State the blood parasite species.
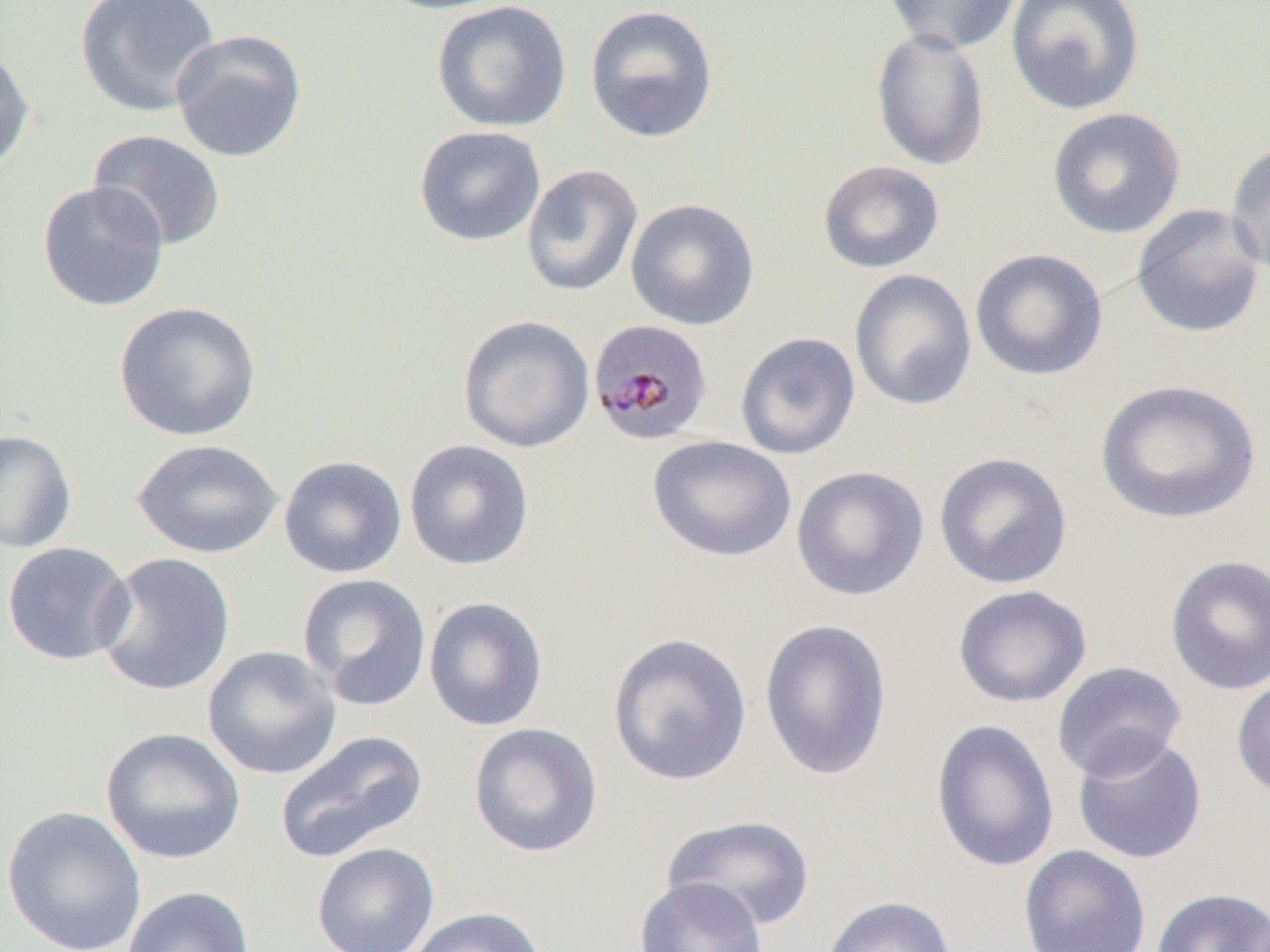

Plasmodium malariae.

modality = optical microscopy
Plasmodium malariae-infected red blood cell locations = approximate bounding boxes as named x1/y1/x2/y2 corners in pixels: (x1=588, y1=319, x2=714, y2=446)
field of view = single
preparation = thin blood smear
image size = 1270×952 pixels
magnification = 1000x
uninfected red blood cell locations = approximate bounding boxes as named x1/y1/x2/y2 corners in pixels: (x1=75, y1=0, x2=221, y2=117), (x1=371, y1=0, x2=512, y2=15), (x1=882, y1=0, x2=1023, y2=55), (x1=1005, y1=0, x2=1146, y2=115), (x1=431, y1=1, x2=572, y2=133), (x1=584, y1=4, x2=719, y2=144), (x1=870, y1=26, x2=990, y2=171), (x1=170, y1=29, x2=307, y2=163), (x1=0, y1=43, x2=34, y2=174), (x1=1046, y1=107, x2=1186, y2=239), (x1=414, y1=125, x2=546, y2=247), (x1=88, y1=129, x2=226, y2=251), (x1=1225, y1=139, x2=1270, y2=279), (x1=817, y1=160, x2=945, y2=274), (x1=521, y1=164, x2=643, y2=297), (x1=36, y1=181, x2=170, y2=313), (x1=626, y1=198, x2=760, y2=331), (x1=1131, y1=203, x2=1267, y2=339), (x1=970, y1=248, x2=1108, y2=381), (x1=849, y1=268, x2=977, y2=411), (x1=114, y1=301, x2=261, y2=442), (x1=458, y1=315, x2=595, y2=454), (x1=735, y1=332, x2=861, y2=460), (x1=1094, y1=379, x2=1261, y2=525), (x1=0, y1=429, x2=77, y2=553), (x1=648, y1=435, x2=797, y2=562), (x1=131, y1=438, x2=283, y2=559), (x1=404, y1=439, x2=535, y2=571), (x1=934, y1=451, x2=1073, y2=590), (x1=279, y1=455, x2=407, y2=579), (x1=791, y1=465, x2=929, y2=602), (x1=2, y1=542, x2=135, y2=666), (x1=94, y1=551, x2=236, y2=697), (x1=1165, y1=554, x2=1270, y2=695), (x1=297, y1=573, x2=432, y2=712), (x1=952, y1=584, x2=1092, y2=708), (x1=423, y1=596, x2=549, y2=732), (x1=759, y1=617, x2=893, y2=781), (x1=607, y1=632, x2=753, y2=787), (x1=202, y1=645, x2=342, y2=780), (x1=1051, y1=661, x2=1187, y2=781), (x1=1231, y1=674, x2=1270, y2=801), (x1=930, y1=719, x2=1060, y2=874), (x1=468, y1=722, x2=603, y2=858), (x1=100, y1=727, x2=246, y2=865), (x1=274, y1=729, x2=429, y2=864), (x1=1072, y1=733, x2=1208, y2=865), (x1=1, y1=805, x2=147, y2=952), (x1=661, y1=814, x2=817, y2=932), (x1=311, y1=842, x2=440, y2=952), (x1=1018, y1=845, x2=1151, y2=952), (x1=635, y1=877, x2=768, y2=952), (x1=122, y1=886, x2=255, y2=952), (x1=1150, y1=887, x2=1270, y2=952), (x1=820, y1=895, x2=957, y2=952), (x1=405, y1=906, x2=547, y2=952)